State the blood parasite species.
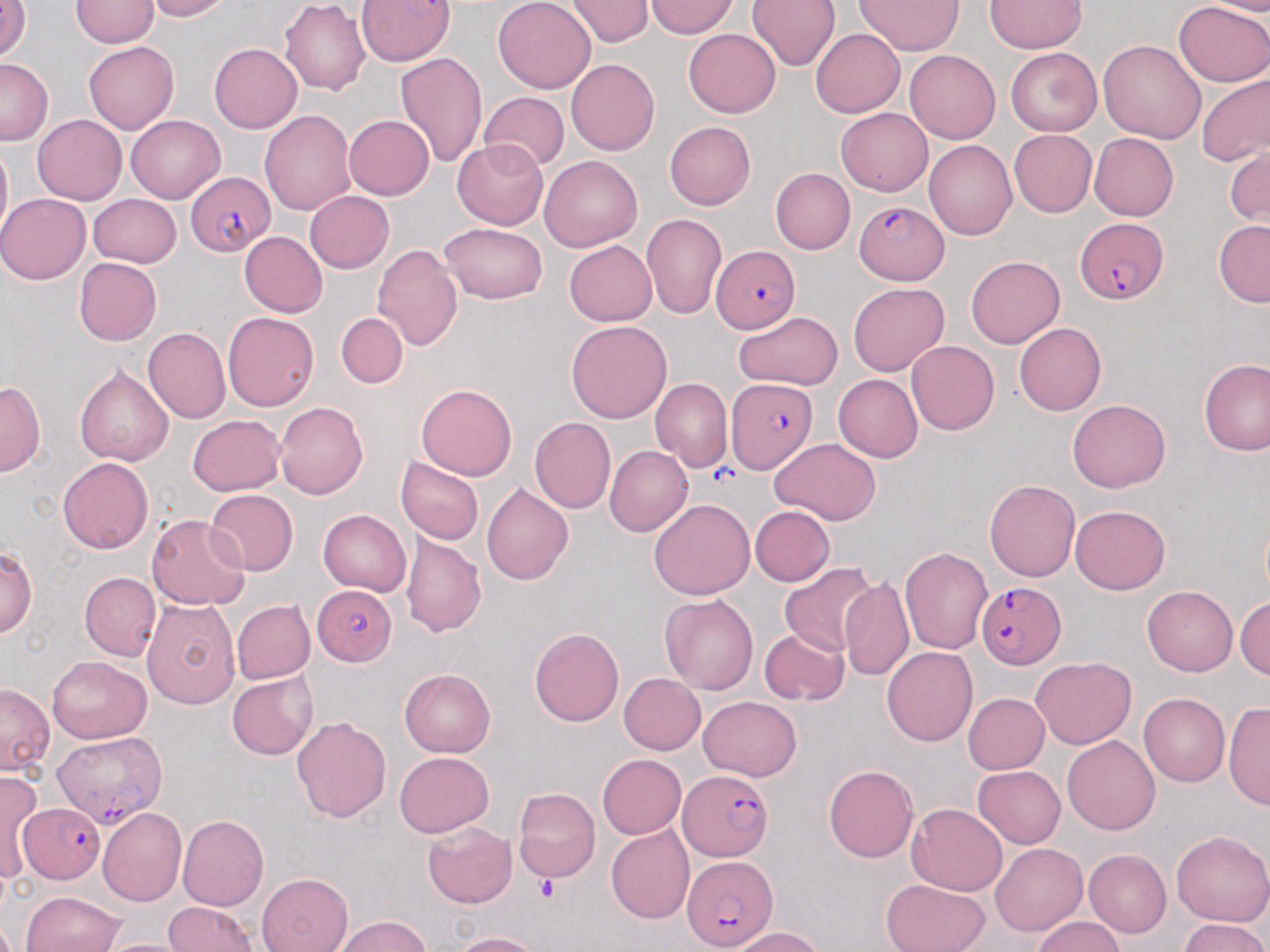

Plasmodium falciparum.

uninfected_red_blood_cell_locations: 'approximate bounding boxes as named x1/y1/x2/y2 corners in pixels: (x1=142, y1=0, x2=233, y2=21), (x1=355, y1=0, x2=455, y2=67), (x1=493, y1=0, x2=595, y2=93), (x1=564, y1=0, x2=655, y2=46), (x1=648, y1=0, x2=738, y2=38), (x1=748, y1=0, x2=839, y2=71), (x1=855, y1=0, x2=965, y2=55), (x1=1199, y1=0, x2=1270, y2=17), (x1=71, y1=1, x2=157, y2=48), (x1=279, y1=1, x2=370, y2=96), (x1=984, y1=1, x2=1087, y2=53), (x1=1173, y1=1, x2=1270, y2=88), (x1=0, y1=3, x2=31, y2=63), (x1=683, y1=29, x2=780, y2=118), (x1=812, y1=29, x2=904, y2=118), (x1=1098, y1=39, x2=1206, y2=142), (x1=84, y1=42, x2=177, y2=134), (x1=209, y1=44, x2=302, y2=133), (x1=1005, y1=47, x2=1102, y2=136), (x1=905, y1=50, x2=1000, y2=144), (x1=394, y1=52, x2=487, y2=167), (x1=0, y1=57, x2=52, y2=145), (x1=566, y1=59, x2=660, y2=156), (x1=1195, y1=72, x2=1270, y2=166), (x1=479, y1=92, x2=569, y2=171), (x1=836, y1=107, x2=932, y2=195), (x1=260, y1=110, x2=356, y2=216), (x1=33, y1=114, x2=126, y2=204), (x1=126, y1=114, x2=224, y2=202), (x1=344, y1=115, x2=434, y2=200), (x1=665, y1=121, x2=756, y2=210), (x1=1009, y1=130, x2=1097, y2=217), (x1=1089, y1=132, x2=1178, y2=221), (x1=0, y1=140, x2=11, y2=242), (x1=451, y1=140, x2=549, y2=230), (x1=925, y1=140, x2=1017, y2=240), (x1=1226, y1=148, x2=1269, y2=228), (x1=540, y1=155, x2=642, y2=251), (x1=770, y1=168, x2=854, y2=255), (x1=305, y1=191, x2=394, y2=273), (x1=0, y1=193, x2=90, y2=284), (x1=88, y1=194, x2=181, y2=268), (x1=641, y1=213, x2=726, y2=320), (x1=1213, y1=220, x2=1270, y2=307), (x1=439, y1=223, x2=548, y2=304), (x1=239, y1=232, x2=327, y2=318), (x1=563, y1=240, x2=657, y2=325), (x1=372, y1=244, x2=463, y2=351), (x1=966, y1=256, x2=1064, y2=347), (x1=73, y1=257, x2=161, y2=345), (x1=848, y1=282, x2=948, y2=376), (x1=732, y1=311, x2=842, y2=390), (x1=336, y1=312, x2=408, y2=388), (x1=223, y1=313, x2=319, y2=411), (x1=566, y1=321, x2=672, y2=423), (x1=1014, y1=322, x2=1106, y2=416), (x1=142, y1=328, x2=230, y2=424), (x1=907, y1=340, x2=1000, y2=435), (x1=1199, y1=359, x2=1269, y2=456), (x1=74, y1=365, x2=173, y2=468), (x1=833, y1=374, x2=923, y2=462), (x1=650, y1=377, x2=733, y2=472), (x1=0, y1=381, x2=46, y2=476), (x1=417, y1=383, x2=517, y2=481), (x1=1067, y1=399, x2=1171, y2=493), (x1=275, y1=400, x2=369, y2=499), (x1=188, y1=415, x2=285, y2=496), (x1=530, y1=417, x2=615, y2=513), (x1=770, y1=438, x2=881, y2=525), (x1=605, y1=446, x2=693, y2=536), (x1=58, y1=457, x2=153, y2=553), (x1=396, y1=457, x2=483, y2=545), (x1=984, y1=480, x2=1081, y2=582), (x1=482, y1=482, x2=574, y2=586), (x1=204, y1=489, x2=299, y2=576), (x1=649, y1=499, x2=755, y2=600), (x1=1070, y1=504, x2=1170, y2=595), (x1=750, y1=505, x2=835, y2=587), (x1=318, y1=509, x2=412, y2=596), (x1=147, y1=513, x2=250, y2=610), (x1=401, y1=533, x2=486, y2=637), (x1=1, y1=545, x2=36, y2=638), (x1=900, y1=545, x2=993, y2=653), (x1=779, y1=563, x2=880, y2=659), (x1=80, y1=572, x2=161, y2=662), (x1=839, y1=578, x2=915, y2=682), (x1=1142, y1=585, x2=1238, y2=676), (x1=659, y1=594, x2=758, y2=695), (x1=1234, y1=595, x2=1270, y2=681), (x1=141, y1=599, x2=240, y2=708), (x1=232, y1=600, x2=315, y2=683), (x1=529, y1=628, x2=623, y2=726), (x1=759, y1=630, x2=849, y2=707), (x1=881, y1=646, x2=977, y2=746), (x1=1032, y1=655, x2=1136, y2=749), (x1=46, y1=656, x2=151, y2=744), (x1=400, y1=667, x2=495, y2=756), (x1=227, y1=671, x2=318, y2=759), (x1=619, y1=673, x2=705, y2=754), (x1=0, y1=683, x2=54, y2=776), (x1=962, y1=693, x2=1049, y2=774), (x1=1138, y1=693, x2=1230, y2=786), (x1=698, y1=696, x2=802, y2=780), (x1=1224, y1=702, x2=1270, y2=813), (x1=292, y1=715, x2=390, y2=822), (x1=1062, y1=736, x2=1160, y2=835), (x1=395, y1=752, x2=493, y2=836), (x1=596, y1=754, x2=685, y2=839), (x1=823, y1=764, x2=919, y2=863), (x1=973, y1=765, x2=1066, y2=847), (x1=0, y1=769, x2=43, y2=882), (x1=512, y1=786, x2=601, y2=884), (x1=906, y1=803, x2=1008, y2=895), (x1=98, y1=807, x2=186, y2=905), (x1=178, y1=815, x2=269, y2=911), (x1=423, y1=823, x2=517, y2=908), (x1=606, y1=825, x2=694, y2=924), (x1=1170, y1=830, x2=1269, y2=926), (x1=992, y1=843, x2=1088, y2=936), (x1=1084, y1=849, x2=1171, y2=938), (x1=258, y1=873, x2=352, y2=952), (x1=881, y1=879, x2=989, y2=952), (x1=21, y1=891, x2=124, y2=952), (x1=164, y1=902, x2=259, y2=952), (x1=1032, y1=915, x2=1124, y2=952), (x1=334, y1=916, x2=430, y2=952), (x1=1178, y1=919, x2=1269, y2=952), (x1=731, y1=927, x2=825, y2=952), (x1=453, y1=931, x2=543, y2=952), (x1=95, y1=938, x2=195, y2=952)'
stain: May-Grünwald-Giemsa
platelet_locations: 'approximate bounding boxes as named x1/y1/x2/y2 corners in pixels: (x1=533, y1=877, x2=559, y2=902)'
magnification: 1000x
field_of_view: single
preparation: thin blood smear
plasmodium_falciparum_infected_red_blood_cell_locations: 'approximate bounding boxes as named x1/y1/x2/y2 corners in pixels: (x1=187, y1=171, x2=275, y2=254), (x1=857, y1=201, x2=953, y2=287), (x1=1076, y1=218, x2=1167, y2=304), (x1=714, y1=248, x2=800, y2=331), (x1=726, y1=379, x2=818, y2=473), (x1=975, y1=580, x2=1065, y2=668), (x1=311, y1=585, x2=396, y2=670), (x1=53, y1=731, x2=167, y2=827), (x1=678, y1=769, x2=772, y2=861), (x1=18, y1=803, x2=106, y2=883), (x1=681, y1=858, x2=777, y2=950)'
modality: optical microscopy
image_size: 1270×952 pixels